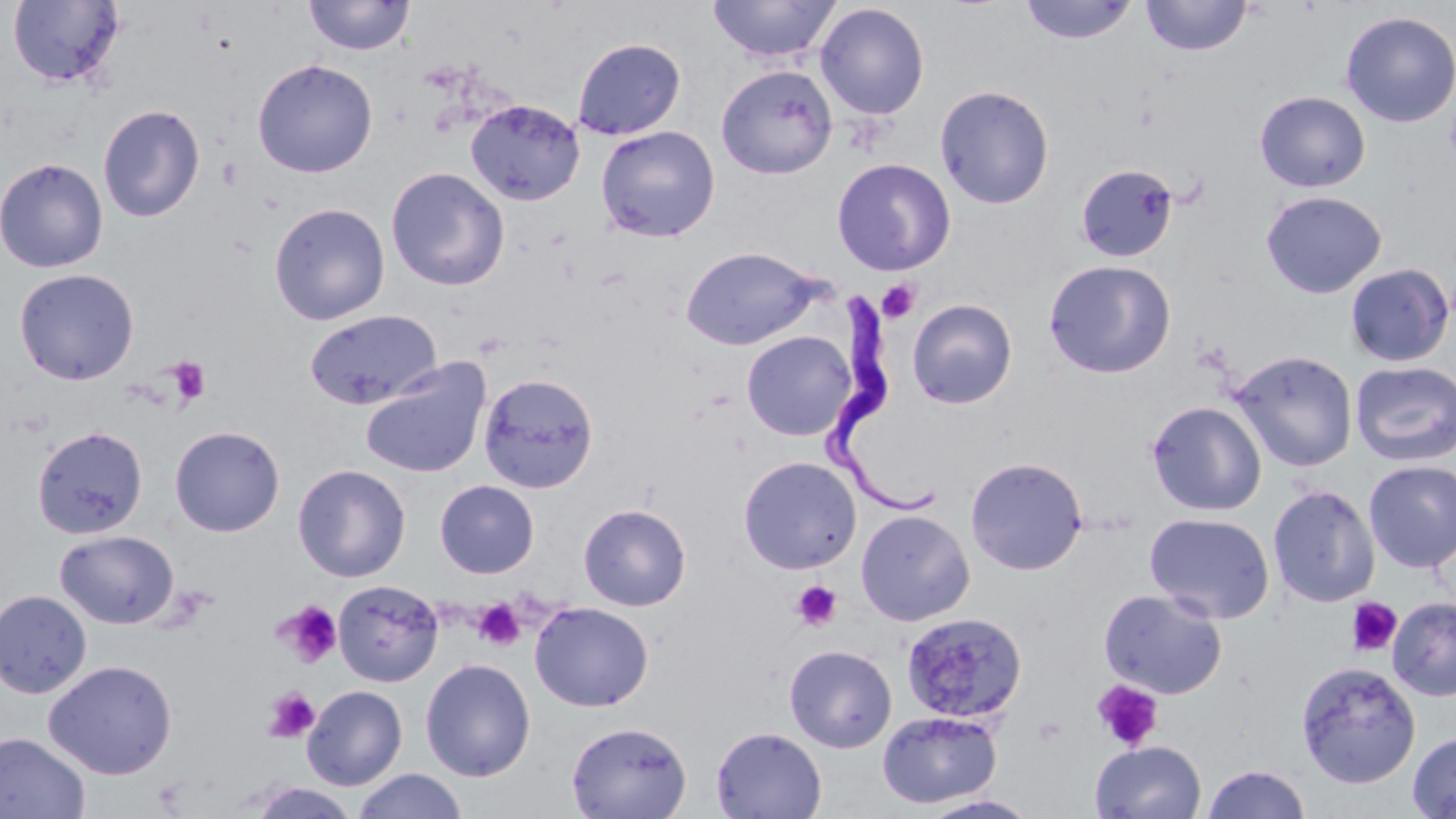

Approximate bounding boxes as named x1/y1/x2/y2 corners in pixels. Uninfected red blood cell locations: (x1=304, y1=0, x2=415, y2=56), (x1=708, y1=0, x2=841, y2=64), (x1=1018, y1=0, x2=1138, y2=45), (x1=1141, y1=0, x2=1252, y2=56), (x1=7, y1=1, x2=126, y2=89), (x1=814, y1=3, x2=930, y2=120), (x1=1340, y1=10, x2=1456, y2=128), (x1=572, y1=37, x2=686, y2=140), (x1=252, y1=58, x2=377, y2=178), (x1=716, y1=64, x2=838, y2=179), (x1=935, y1=85, x2=1055, y2=209), (x1=1254, y1=90, x2=1371, y2=192), (x1=465, y1=99, x2=585, y2=206), (x1=98, y1=104, x2=205, y2=222), (x1=596, y1=125, x2=720, y2=242), (x1=0, y1=157, x2=108, y2=273), (x1=832, y1=157, x2=956, y2=276), (x1=1075, y1=163, x2=1179, y2=263), (x1=386, y1=167, x2=510, y2=291), (x1=1260, y1=190, x2=1387, y2=298), (x1=269, y1=202, x2=390, y2=326), (x1=680, y1=245, x2=825, y2=350), (x1=1043, y1=259, x2=1177, y2=379), (x1=1344, y1=262, x2=1454, y2=367), (x1=14, y1=268, x2=139, y2=384), (x1=907, y1=298, x2=1018, y2=409), (x1=304, y1=308, x2=443, y2=410), (x1=741, y1=330, x2=857, y2=442), (x1=1229, y1=349, x2=1358, y2=472), (x1=359, y1=358, x2=491, y2=479), (x1=1351, y1=360, x2=1456, y2=467), (x1=478, y1=372, x2=599, y2=494), (x1=1146, y1=400, x2=1267, y2=516), (x1=170, y1=425, x2=285, y2=537), (x1=32, y1=426, x2=148, y2=539), (x1=738, y1=455, x2=862, y2=574), (x1=965, y1=456, x2=1088, y2=575), (x1=1363, y1=460, x2=1456, y2=573), (x1=293, y1=464, x2=410, y2=582), (x1=434, y1=480, x2=539, y2=578), (x1=1268, y1=484, x2=1380, y2=608), (x1=578, y1=504, x2=691, y2=611), (x1=855, y1=509, x2=975, y2=626), (x1=1144, y1=511, x2=1275, y2=623), (x1=54, y1=529, x2=179, y2=628), (x1=333, y1=580, x2=443, y2=686), (x1=1098, y1=588, x2=1228, y2=699), (x1=0, y1=590, x2=92, y2=698), (x1=1388, y1=597, x2=1456, y2=701), (x1=529, y1=601, x2=654, y2=711), (x1=901, y1=612, x2=1027, y2=724), (x1=784, y1=644, x2=897, y2=753), (x1=420, y1=658, x2=536, y2=782), (x1=44, y1=660, x2=176, y2=779), (x1=1296, y1=660, x2=1420, y2=788), (x1=302, y1=685, x2=407, y2=790), (x1=876, y1=710, x2=1002, y2=808), (x1=566, y1=720, x2=691, y2=819), (x1=711, y1=726, x2=827, y2=819), (x1=1407, y1=731, x2=1456, y2=818), (x1=0, y1=732, x2=91, y2=819), (x1=1090, y1=740, x2=1207, y2=819), (x1=1201, y1=764, x2=1312, y2=819), (x1=352, y1=769, x2=468, y2=819), (x1=248, y1=783, x2=360, y2=818), (x1=918, y1=794, x2=1042, y2=819). Trypanosoma brucei locations: (x1=823, y1=288, x2=940, y2=517). Platelet locations: (x1=877, y1=280, x2=920, y2=324), (x1=168, y1=357, x2=211, y2=406), (x1=792, y1=581, x2=843, y2=631), (x1=1345, y1=596, x2=1403, y2=658), (x1=473, y1=599, x2=526, y2=652), (x1=275, y1=600, x2=343, y2=668), (x1=1091, y1=679, x2=1164, y2=752), (x1=264, y1=687, x2=320, y2=742). Slide-level diagnosis: Trypanosoma brucei. Captured at 1000x magnification. Image is 1456×819 pixels. May-Grünwald-Giemsa-stained preparation. Thin blood smear. One field of a larger specimen. Light microscopy.